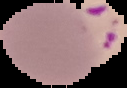
Summary:
  - Image size: 127×88 pixels
  - Image type: segmented cell region with the area outside set to black
  - Result: Plasmodium parasites detected
  - Preparation: thin blood film